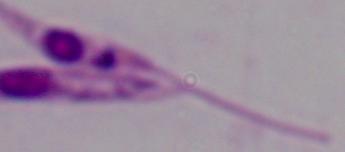 1000x magnification. A Leishmania parasite is seen. Photomicrograph.